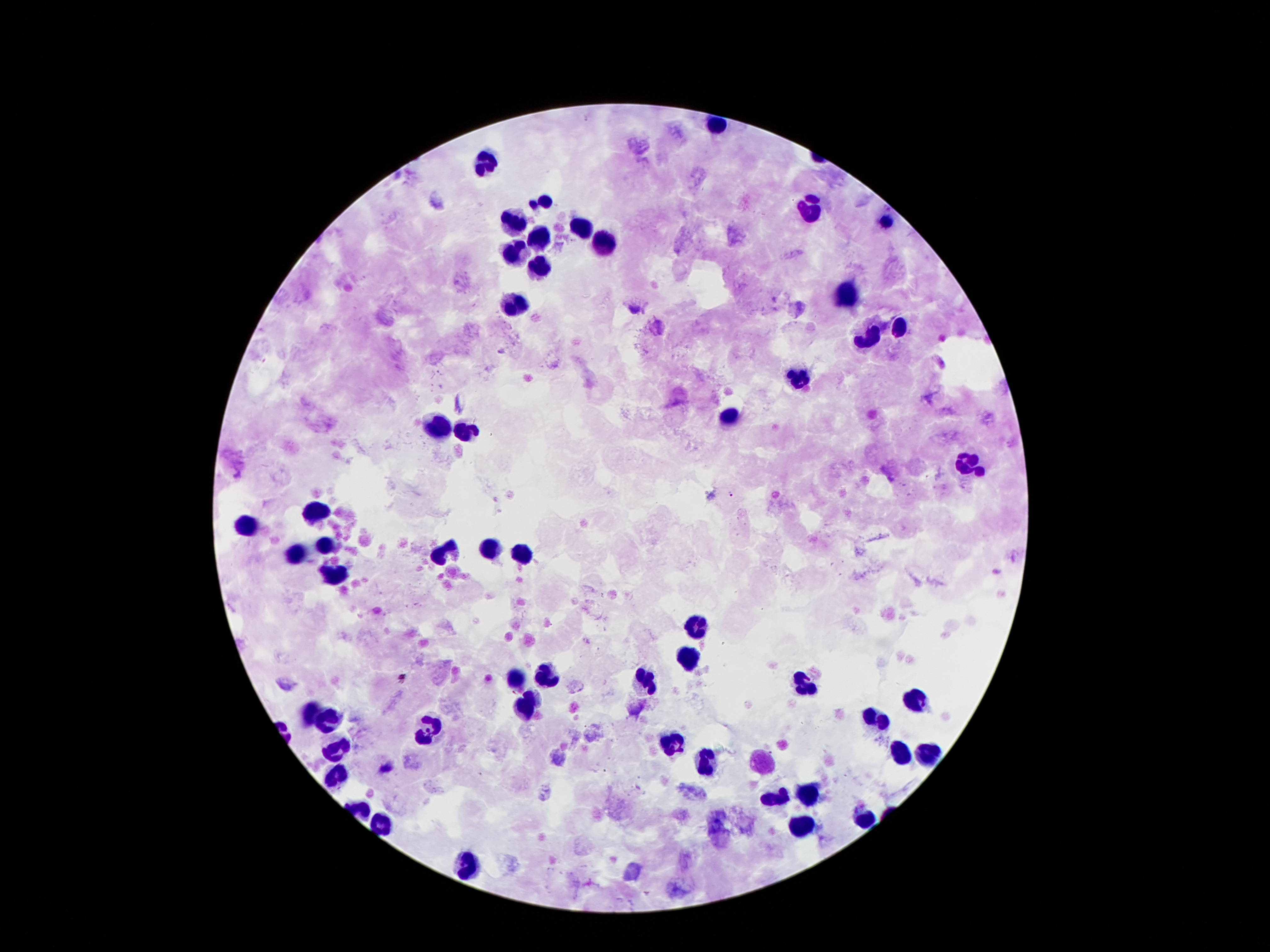
Approximate object centers, in pixels from the top-left corner.
Summary:
  - Malaria parasite locations: (x=732, y=495), (x=402, y=677)
  - Leukocyte locations: (x=483, y=162), (x=547, y=201), (x=810, y=211), (x=512, y=219), (x=888, y=221), (x=585, y=229), (x=539, y=239), (x=603, y=243), (x=516, y=255), (x=539, y=267), (x=847, y=296), (x=511, y=307), (x=899, y=328), (x=868, y=338), (x=802, y=376), (x=728, y=417), (x=441, y=427), (x=466, y=429), (x=969, y=463), (x=316, y=514), (x=247, y=525), (x=326, y=547), (x=489, y=547), (x=300, y=552), (x=441, y=554), (x=522, y=554), (x=333, y=572), (x=697, y=625), (x=689, y=659), (x=547, y=673), (x=646, y=679), (x=516, y=682), (x=802, y=687), (x=916, y=701), (x=524, y=705), (x=311, y=712), (x=875, y=718), (x=329, y=720), (x=430, y=726), (x=670, y=746), (x=339, y=751), (x=922, y=752), (x=899, y=755), (x=703, y=762), (x=338, y=776), (x=810, y=796), (x=779, y=801), (x=862, y=819), (x=385, y=820), (x=804, y=825), (x=468, y=862)
  - Capture: smartphone camera through the microscope eyepiece
  - Preparation: thick peripheral-blood smear
  - Patient malaria status: infected with Plasmodium falciparum
  - Magnification: 100x
  - Stain: Giemsa
  - Image size: 1270×952 pixels
  - Field of view: one from this slide